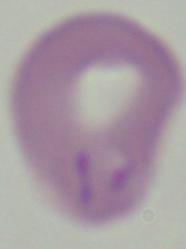
A Babesia parasite is shown. Photomicrograph. Captured at 1000x magnification.